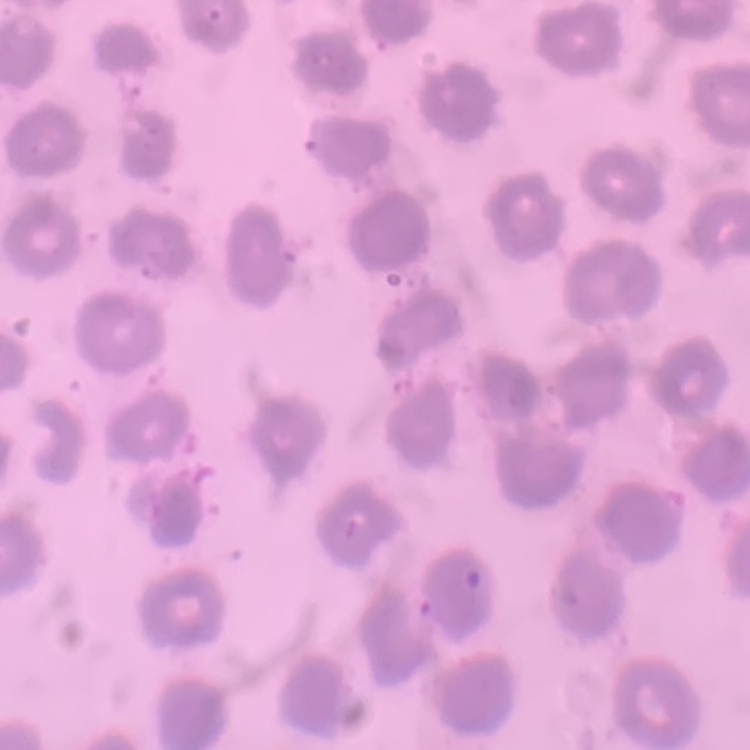
red blood cell morphology = no rouleaux formation
preparation = thin blood smear
stain = Field's or Giemsa
image type = one tile cut from a larger photomicrograph